State which parasite is depicted.
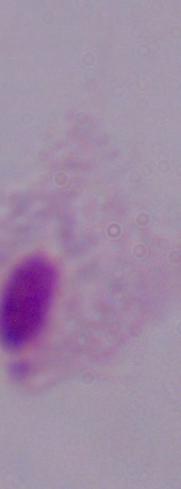
A trichomonad.

Summary:
  - Magnification: 1000x
  - Modality: micrograph